Name the parasite shown.
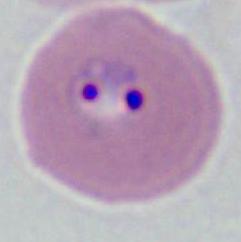

This is Plasmodium.

400x or 1000x magnification. Photomicrograph.